State which parasite is depicted.
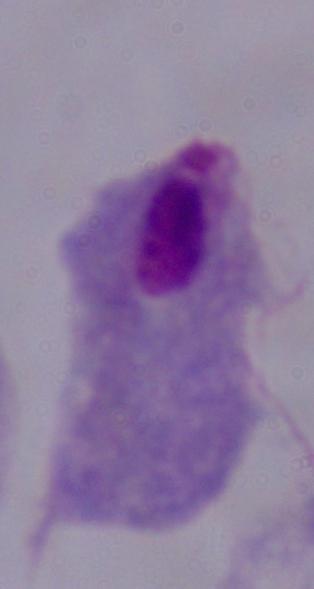
A trichomonad.

Summary:
  - Modality: photomicrograph
  - Magnification: 1000x